Assess this cell for malaria.
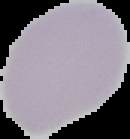

It is uninfected.

Summary:
  - Preparation: thin blood smear
  - Image size: 130×139 pixels
  - Image type: cell region segmented out of the field of view; surrounding area masked to black